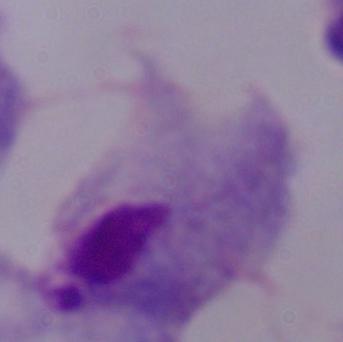
modality = photomicrograph
magnification = 1000x
identification = trichomonad